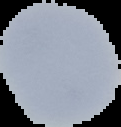

Summary:
  - Image size: 121×127 pixels
  - Result: no Plasmodium parasites detected
  - Preparation: thin blood smear
  - Image type: segmented cell region with the area outside set to black